Assess the morphology of the red blood cells.
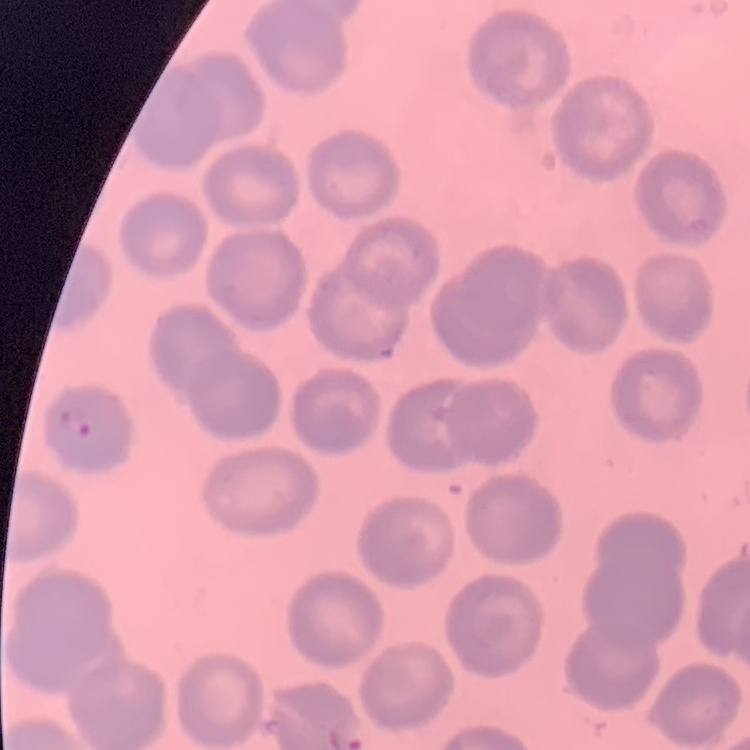
They show no rouleaux formation.

Summary:
  - Image type: one tile cut from a larger photomicrograph
  - Preparation: thin blood smear
  - Stain: Field's or Giemsa